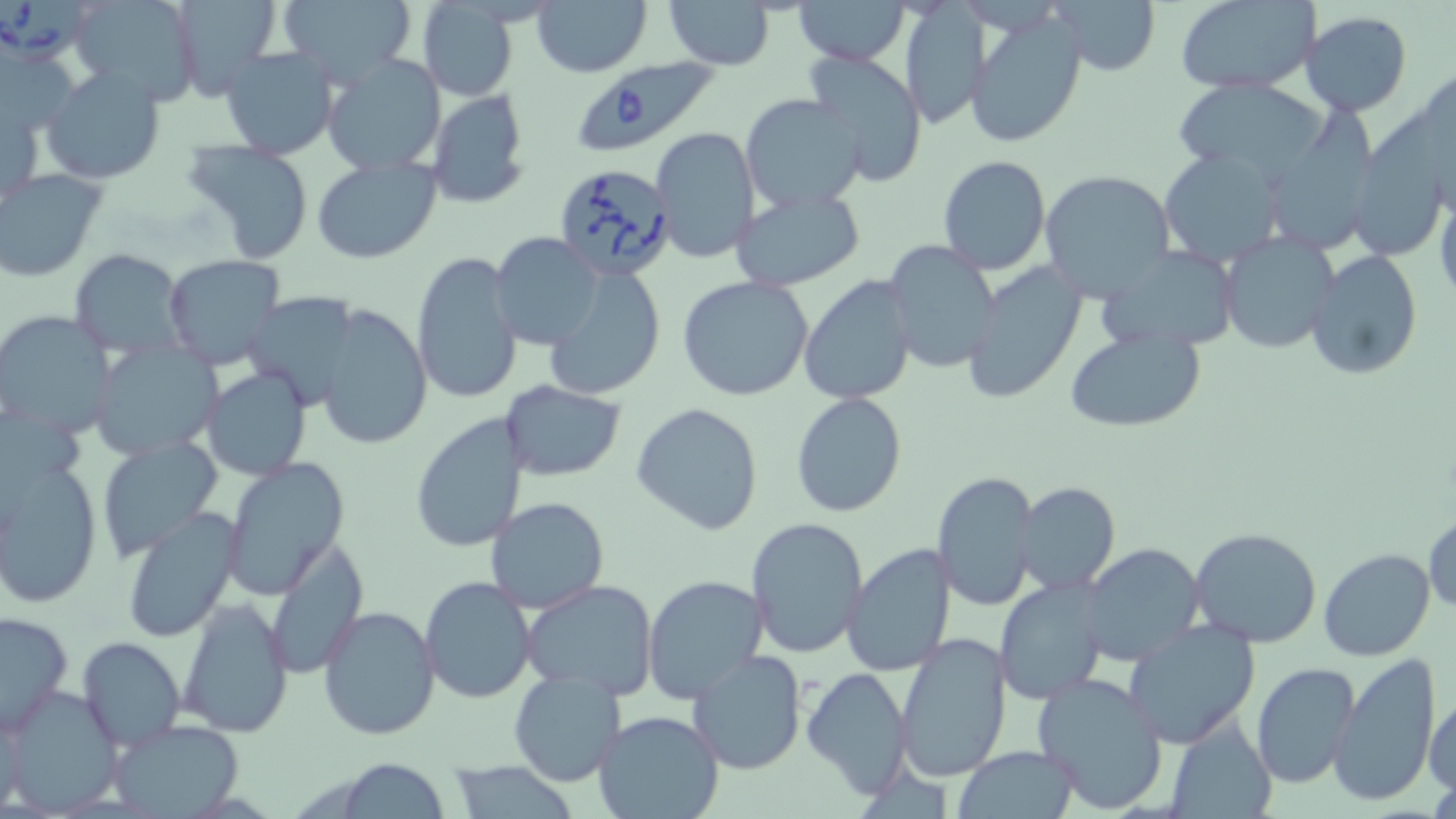
slide-level diagnosis = Babesia divergens
stain = May-Grünwald-Giemsa
modality = light microscopy
field of view = single
preparation = thin blood film
uninfected red blood cell locations = approximate bounding boxes as named x1/y1/x2/y2 corners in pixels: (x1=70, y1=0, x2=201, y2=106), (x1=168, y1=0, x2=283, y2=102), (x1=276, y1=0, x2=419, y2=85), (x1=532, y1=0, x2=654, y2=78), (x1=663, y1=0, x2=777, y2=70), (x1=794, y1=0, x2=910, y2=65), (x1=1173, y1=0, x2=1320, y2=94), (x1=1049, y1=1, x2=1161, y2=76), (x1=898, y1=2, x2=987, y2=130), (x1=414, y1=5, x2=518, y2=100), (x1=968, y1=10, x2=1088, y2=149), (x1=1300, y1=11, x2=1413, y2=115), (x1=0, y1=46, x2=80, y2=141), (x1=218, y1=46, x2=340, y2=162), (x1=801, y1=50, x2=929, y2=187), (x1=321, y1=55, x2=447, y2=176), (x1=1411, y1=57, x2=1456, y2=210), (x1=41, y1=66, x2=166, y2=184), (x1=1172, y1=76, x2=1331, y2=185), (x1=426, y1=88, x2=531, y2=208), (x1=2, y1=91, x2=46, y2=210), (x1=740, y1=93, x2=868, y2=212), (x1=1273, y1=96, x2=1378, y2=255), (x1=1344, y1=110, x2=1441, y2=266), (x1=649, y1=126, x2=760, y2=263), (x1=182, y1=138, x2=316, y2=264), (x1=1158, y1=150, x2=1285, y2=268), (x1=937, y1=155, x2=1051, y2=274), (x1=312, y1=156, x2=441, y2=263), (x1=1039, y1=168, x2=1176, y2=301), (x1=0, y1=169, x2=108, y2=281), (x1=1432, y1=177, x2=1456, y2=303), (x1=730, y1=186, x2=867, y2=291), (x1=1217, y1=230, x2=1340, y2=353), (x1=490, y1=232, x2=603, y2=351), (x1=881, y1=241, x2=1001, y2=375), (x1=1100, y1=246, x2=1239, y2=350), (x1=1304, y1=248, x2=1424, y2=380), (x1=69, y1=249, x2=185, y2=357), (x1=410, y1=251, x2=523, y2=406), (x1=162, y1=255, x2=287, y2=372), (x1=959, y1=261, x2=1089, y2=405), (x1=543, y1=266, x2=666, y2=401), (x1=677, y1=275, x2=814, y2=400), (x1=799, y1=275, x2=919, y2=405), (x1=316, y1=305, x2=431, y2=449), (x1=0, y1=309, x2=116, y2=440), (x1=1064, y1=326, x2=1207, y2=434), (x1=89, y1=341, x2=221, y2=460), (x1=200, y1=367, x2=312, y2=481), (x1=500, y1=381, x2=626, y2=482), (x1=791, y1=392, x2=907, y2=516), (x1=631, y1=403, x2=764, y2=536), (x1=411, y1=412, x2=528, y2=551), (x1=95, y1=435, x2=222, y2=562), (x1=0, y1=457, x2=102, y2=608), (x1=221, y1=459, x2=350, y2=600), (x1=932, y1=467, x2=1039, y2=613), (x1=1014, y1=482, x2=1121, y2=596), (x1=484, y1=496, x2=609, y2=612), (x1=119, y1=506, x2=243, y2=643), (x1=1424, y1=511, x2=1455, y2=616), (x1=746, y1=517, x2=869, y2=659), (x1=1190, y1=526, x2=1324, y2=647), (x1=265, y1=537, x2=368, y2=680), (x1=841, y1=542, x2=958, y2=678), (x1=1082, y1=543, x2=1206, y2=668), (x1=1319, y1=547, x2=1435, y2=661), (x1=641, y1=574, x2=770, y2=702), (x1=419, y1=575, x2=537, y2=704), (x1=521, y1=579, x2=661, y2=700), (x1=994, y1=579, x2=1107, y2=705), (x1=177, y1=599, x2=294, y2=737), (x1=318, y1=603, x2=441, y2=742), (x1=1, y1=610, x2=74, y2=734), (x1=1122, y1=621, x2=1261, y2=750), (x1=894, y1=633, x2=1012, y2=782), (x1=78, y1=637, x2=186, y2=752), (x1=686, y1=651, x2=810, y2=775), (x1=1330, y1=652, x2=1442, y2=807), (x1=1249, y1=662, x2=1359, y2=787), (x1=801, y1=665, x2=914, y2=800), (x1=508, y1=668, x2=628, y2=788), (x1=1031, y1=672, x2=1169, y2=812), (x1=2, y1=684, x2=123, y2=815), (x1=1425, y1=695, x2=1456, y2=799), (x1=592, y1=710, x2=726, y2=819), (x1=1166, y1=716, x2=1275, y2=818), (x1=106, y1=719, x2=246, y2=818), (x1=951, y1=745, x2=1082, y2=818), (x1=334, y1=759, x2=455, y2=817), (x1=446, y1=760, x2=583, y2=817)
image size = 1456×819 pixels
Babesia divergens-infected red blood cell locations = approximate bounding boxes as named x1/y1/x2/y2 corners in pixels: (x1=0, y1=0, x2=98, y2=61), (x1=571, y1=57, x2=717, y2=156), (x1=553, y1=162, x2=679, y2=283)
magnification = 1000x